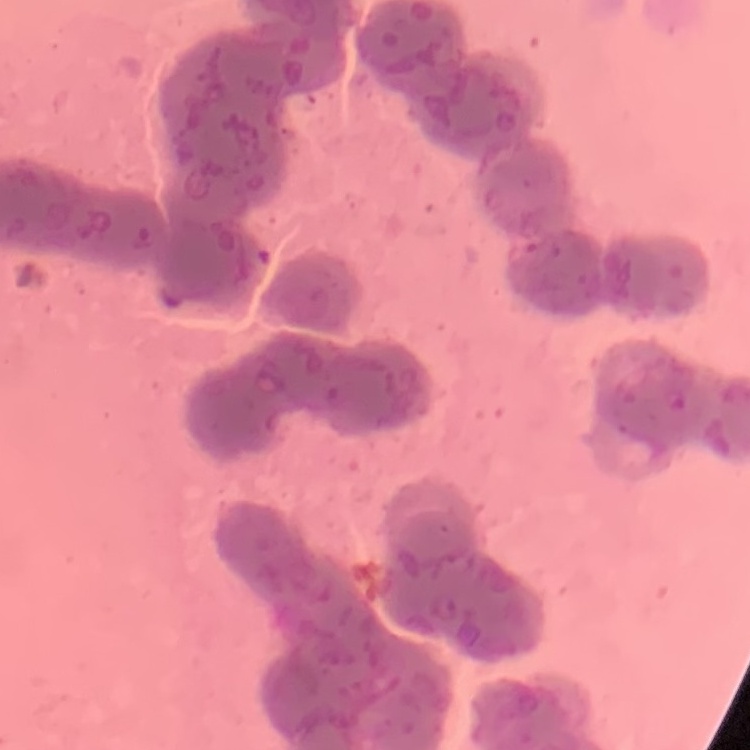
The erythrocytes exhibit rouleaux formation. Thin blood smear. Stained with either Field's or Giemsa. Square crop of a larger photomicrograph.